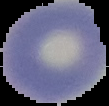

result = negative for Plasmodium parasites
preparation = thin blood film
image size = 109×106 pixels
image type = segmented cell region with the area outside set to black